Report the malaria status of this cell.
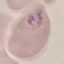

It is parasitized.

capture = smartphone through the microscope eyepiece
image type = automatically extracted cell patch, resized to 64 × 64 pixels
preparation = thin smear
stain = Giemsa